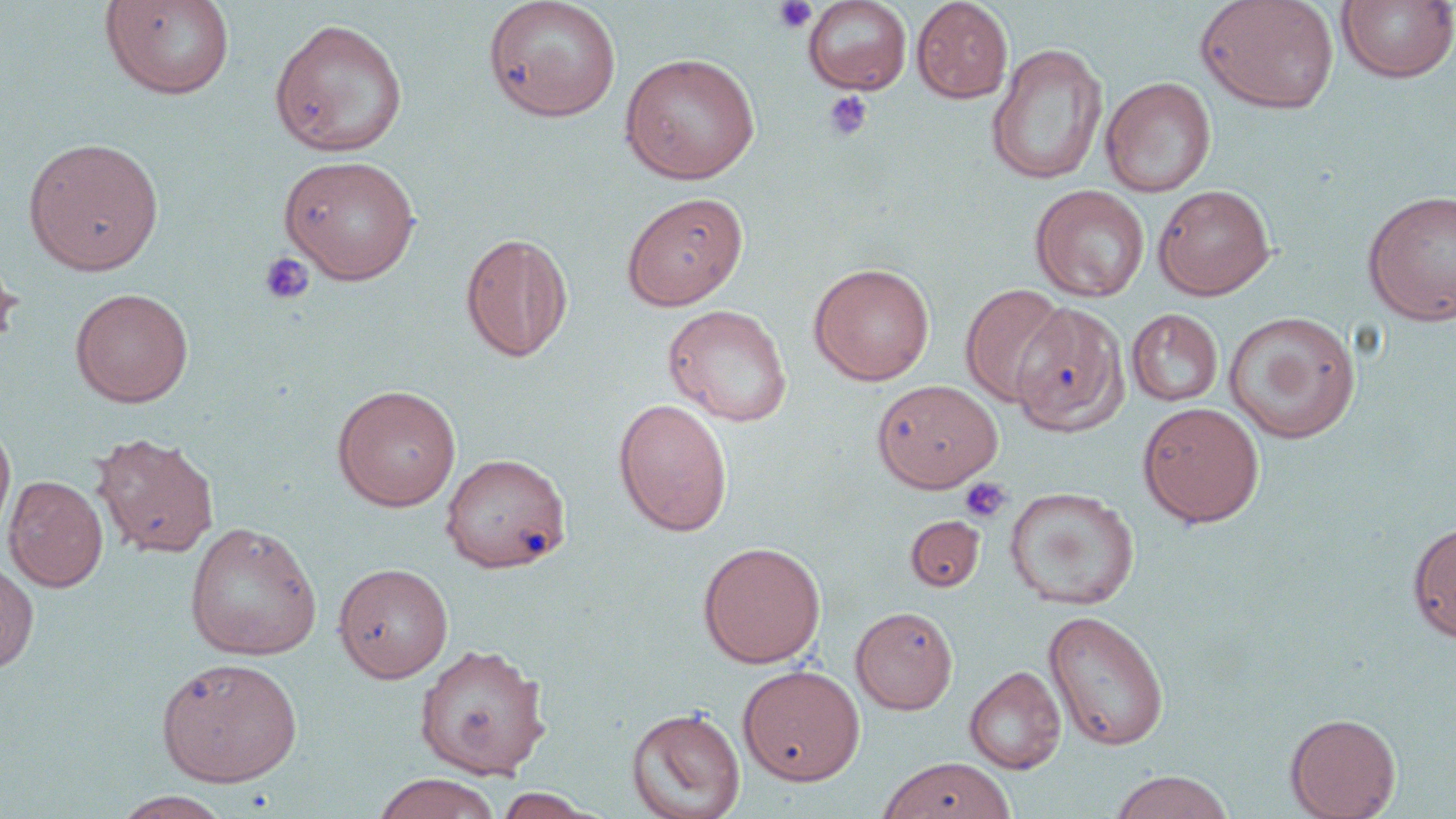
Summary:
  - Coordinate format: approximate bounding boxes as (x1,y1)-(x2,y2) corner pairs in pixels
  - Uninfected red blood cell locations: (99,0)-(236,100), (803,0)-(912,95), (911,0)-(1013,103), (1195,0)-(1340,114), (483,1)-(622,122), (1336,1)-(1456,84), (269,18)-(409,157), (986,43)-(1108,186), (619,52)-(760,184), (1101,77)-(1216,197), (23,136)-(164,275), (278,154)-(422,284), (1153,184)-(1275,300), (1030,185)-(1150,302), (1362,190)-(1456,326), (620,191)-(748,310), (460,231)-(574,363), (0,253)-(21,354), (809,262)-(935,385), (960,284)-(1069,407), (69,287)-(193,408), (983,299)-(1127,430), (663,304)-(793,427), (1126,308)-(1223,406), (1223,311)-(1361,443), (872,379)-(1003,492), (332,384)-(462,511), (613,397)-(733,537), (1137,401)-(1265,527), (0,420)-(16,546), (91,432)-(220,558), (439,452)-(571,573), (3,475)-(108,592), (1004,486)-(1140,611), (905,515)-(985,591), (1407,520)-(1456,642), (184,521)-(322,660), (697,541)-(826,669), (0,558)-(38,673), (333,562)-(454,683), (850,606)-(958,714), (1043,610)-(1170,751), (413,642)-(551,780), (155,656)-(304,787), (737,664)-(865,786), (964,666)-(1066,774), (625,706)-(746,819), (1285,712)-(1401,819), (877,756)-(1016,819), (1108,770)-(1235,819), (372,773)-(502,819), (491,788)-(605,819), (111,791)-(234,818)
  - Platelet locations: (772,0)-(817,34), (822,91)-(873,142), (260,252)-(315,305), (958,476)-(1013,524)
  - Slide-level diagnosis: negative for blood parasites
  - Image size: 1456×819 pixels
  - Preparation: thin blood film
  - Field of view: single
  - Stain: May-Grünwald-Giemsa
  - Magnification: 1000x
  - Modality: light microscopy